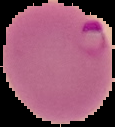
From a thin blood smear. Segmented cell region on a black background. Image is 115×127 pixels. Result: malaria parasites identified.